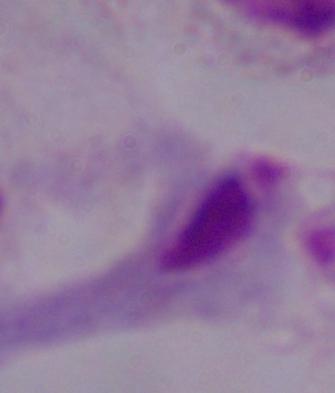

identification = trichomonad
magnification = 1000x
modality = micrograph